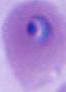

Summary:
  - Modality: micrograph
  - Identification: Plasmodium
  - Magnification: 400x or 1000x